Name the parasite shown.
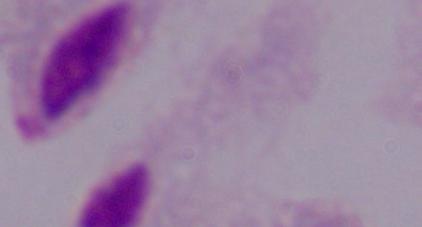
This is a trichomonad.

{
  "magnification": "1000x",
  "modality": "photomicrograph"
}